Name the parasite shown.
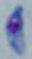
Toxoplasma gondii.

modality = photomicrograph
magnification = 1000x